Assess this cell for malaria.
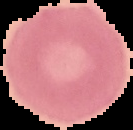

It is uninfected.

Image is 133×130 pixels. Segmented cell region on a black background. From a thin blood smear.